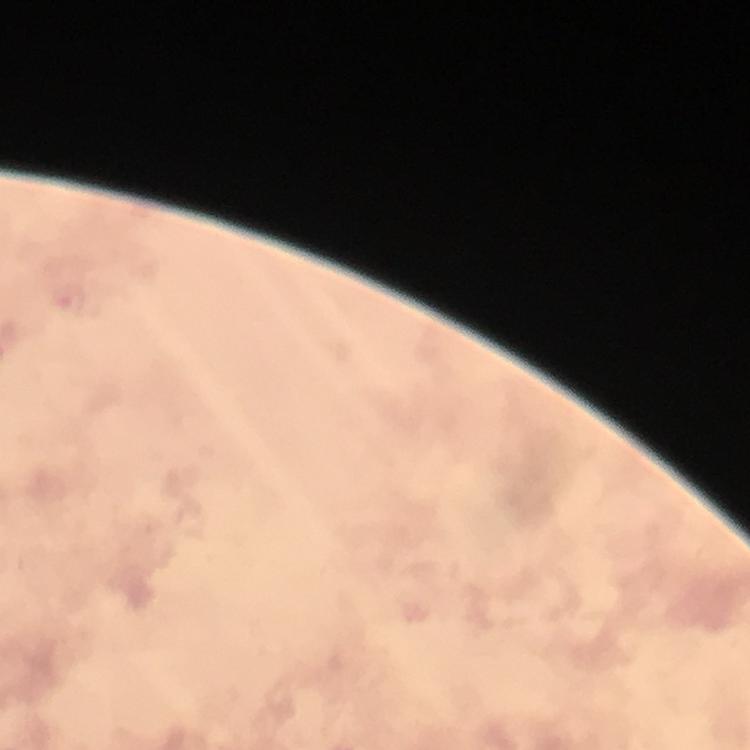
Approximate centers as (x, y) in pixels.
Summary:
  - Malaria parasite locations: (69, 298)
  - Context: from a diagnostic examination for malaria
  - Immersion oil: applied
  - Magnification: 100x
  - Preparation: thick blood smear
  - Cropped from: one field of view
  - Stain: Giemsa
  - Capture: smartphone camera through the microscope
  - Image size: 750×750 pixels